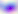
Captured at 400x magnification. Toxoplasma gondii is seen. Micrograph.